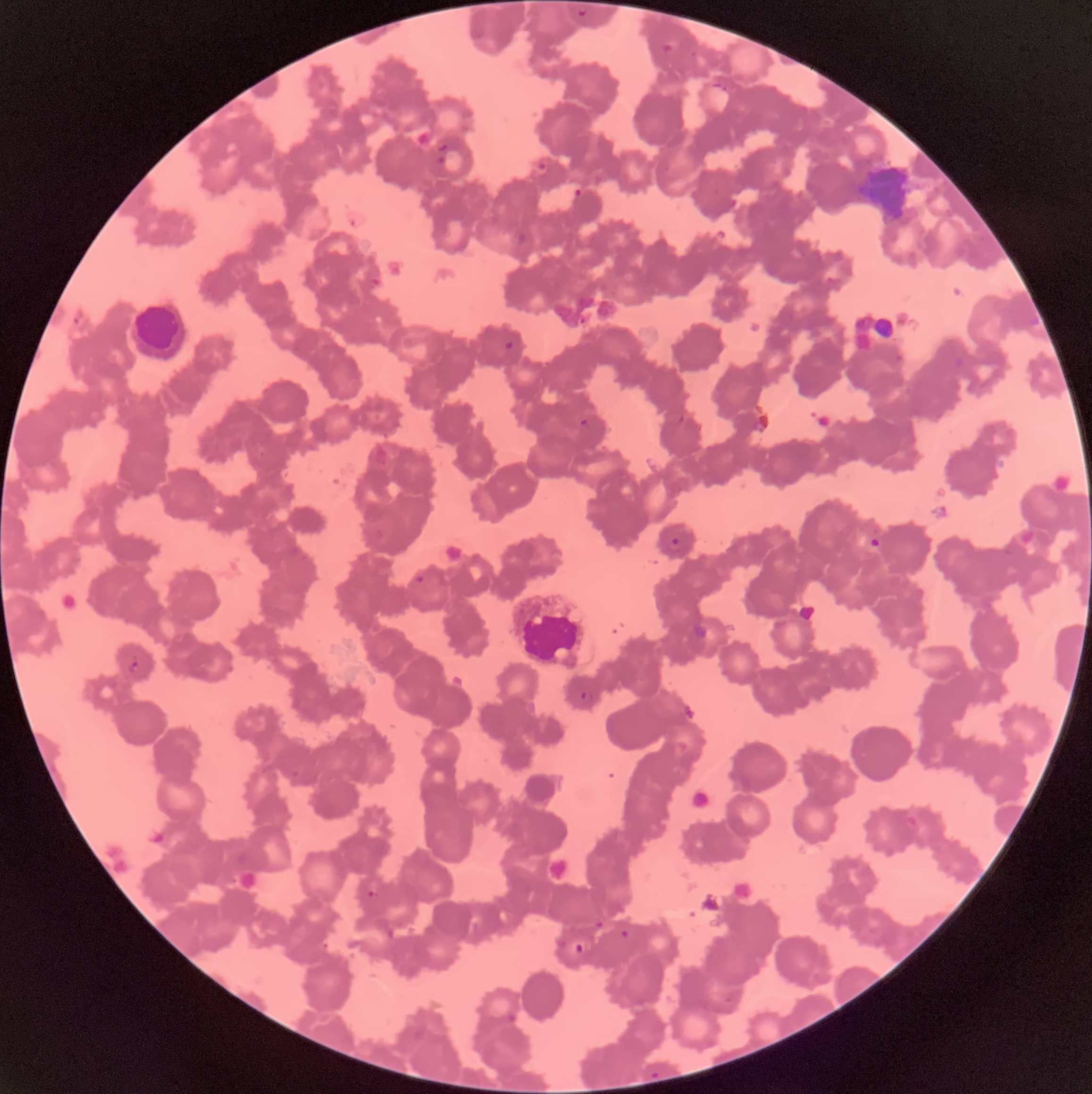

Approximate bounding boxes as (x1,y1)-(x2,y2) corner pairs in pixels. Plasmodium parasite locations: (576,7)-(588,16), (662,38)-(682,55), (711,82)-(728,93), (436,143)-(448,154), (436,156)-(445,164), (536,162)-(548,174), (573,187)-(584,197), (504,339)-(516,351), (578,418)-(590,429), (666,534)-(680,552), (868,535)-(882,553), (412,573)-(426,584), (129,660)-(140,673), (580,690)-(593,704), (288,768)-(300,778), (369,880)-(379,898), (593,920)-(605,929), (618,929)-(629,938), (570,940)-(589,956), (723,996)-(734,1004), (505,1012)-(517,1023), (650,1072)-(661,1080). The red blood cells show rouleaux formation. Thin blood film. Optical microscopy. Image is 1092×1094 pixels.